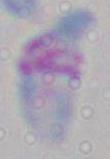 1000x magnification. Micrograph. Toxoplasma gondii is seen.